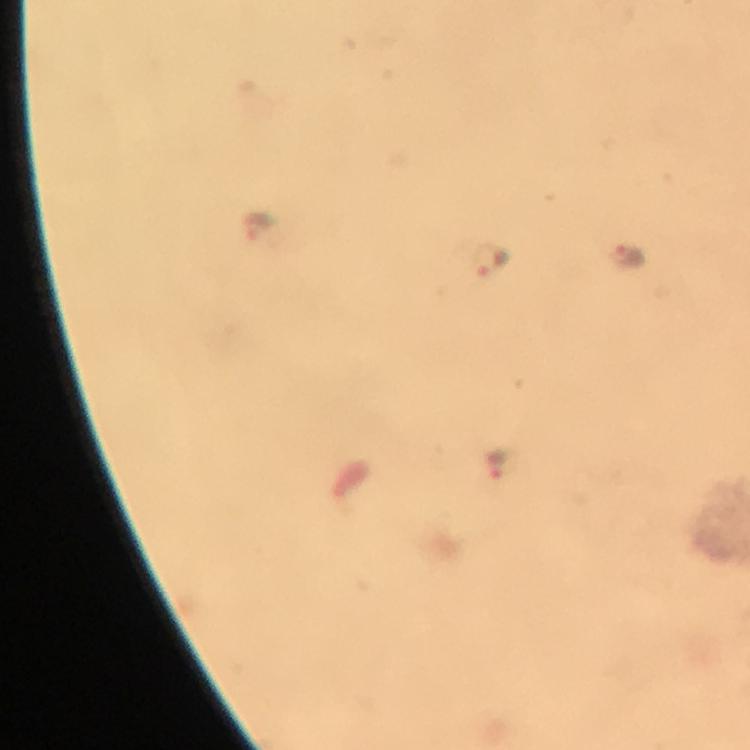
Approximate centers as [x, y] in pixels.
Summary:
  - Malaria parasite locations: [260, 223], [626, 256], [492, 260], [494, 466]
  - Magnification: 100x
  - Immersion oil: applied
  - Preparation: thick smear
  - Image size: 750×750 pixels
  - Cropped from: a single field of view
  - Stain: Giemsa
  - Context: from a diagnostic examination for malaria
  - Capture: smartphone mounted on the microscope